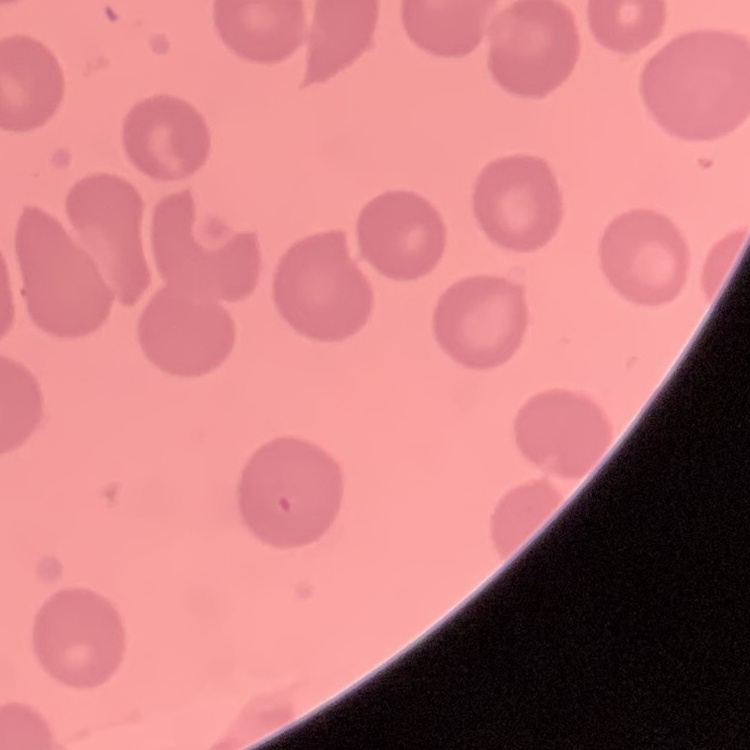

Summary:
  - Erythrocyte morphology: no rouleaux formation
  - Stain: Field's or Giemsa
  - Preparation: thin peripheral smear
  - Image type: square crop of a larger photomicrograph